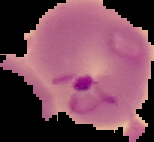

From a thin blood smear. Image is 154×142 pixels. Segmented cell region on a black background. Malaria status: parasitized.